Report the malaria status of this cell.
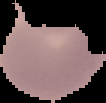

Uninfected.

Summary:
  - Image type: segmented cell region on a black background
  - Image size: 106×103 pixels
  - Preparation: thin blood smear